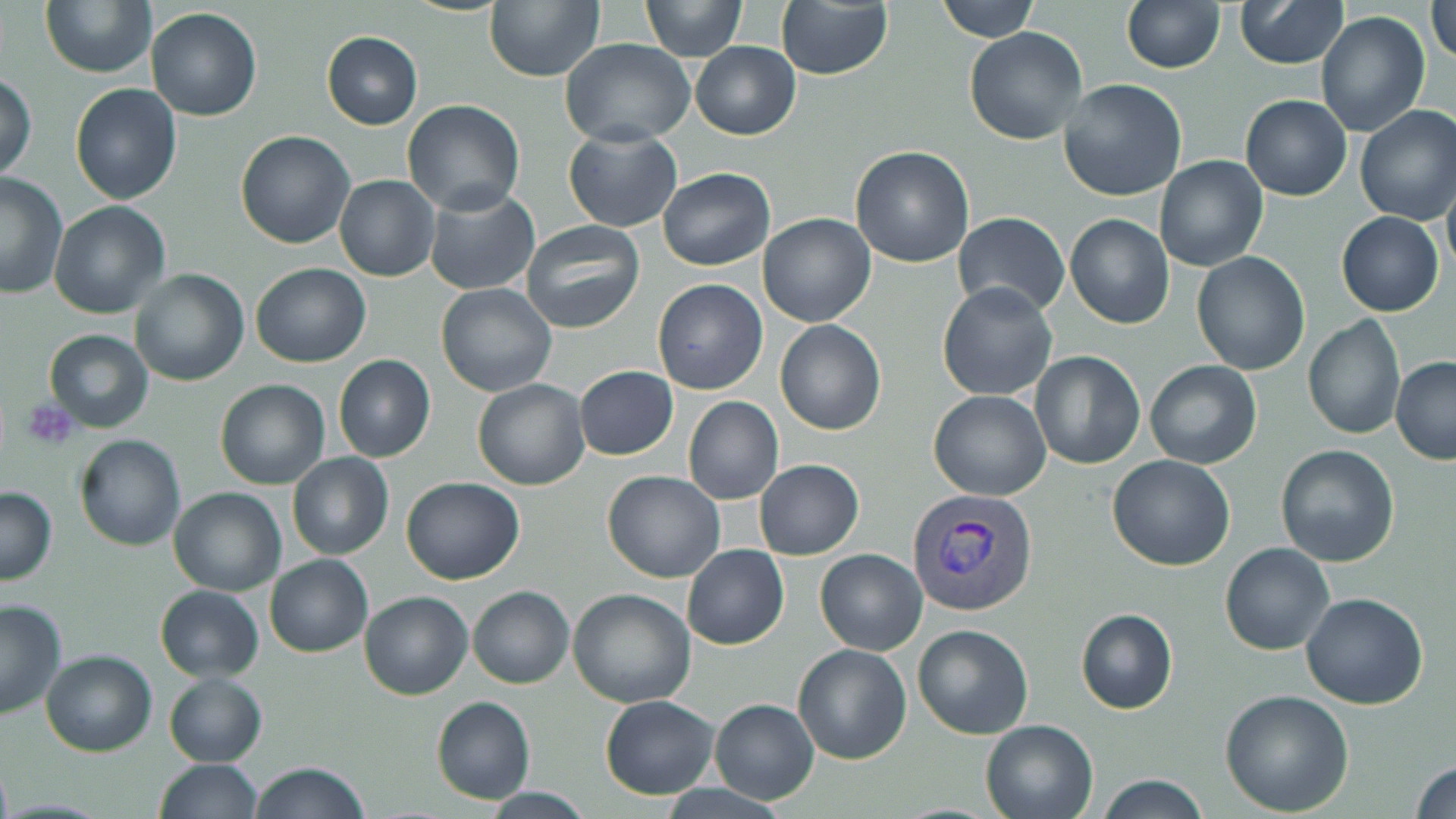

Approximate bounding boxes as named x1/y1/x2/y2 corners in pixels. Platelet locations: (x1=24, y1=401, x2=80, y2=448). Plasmodium vivax-infected red blood cell locations: (x1=905, y1=487, x2=1039, y2=617). Uninfected red blood cell locations: (x1=483, y1=0, x2=604, y2=82), (x1=641, y1=0, x2=745, y2=60), (x1=774, y1=0, x2=892, y2=80), (x1=935, y1=0, x2=1038, y2=41), (x1=1234, y1=0, x2=1347, y2=68), (x1=40, y1=1, x2=155, y2=78), (x1=1121, y1=1, x2=1225, y2=73), (x1=1430, y1=4, x2=1456, y2=62), (x1=145, y1=7, x2=263, y2=122), (x1=1316, y1=11, x2=1428, y2=136), (x1=965, y1=28, x2=1088, y2=146), (x1=321, y1=32, x2=423, y2=129), (x1=561, y1=39, x2=695, y2=148), (x1=690, y1=40, x2=801, y2=140), (x1=0, y1=73, x2=37, y2=180), (x1=1058, y1=79, x2=1188, y2=202), (x1=70, y1=83, x2=183, y2=205), (x1=1240, y1=94, x2=1352, y2=201), (x1=403, y1=100, x2=526, y2=217), (x1=1354, y1=104, x2=1456, y2=225), (x1=564, y1=128, x2=682, y2=232), (x1=234, y1=130, x2=356, y2=249), (x1=850, y1=145, x2=975, y2=267), (x1=1154, y1=156, x2=1268, y2=272), (x1=658, y1=166, x2=775, y2=271), (x1=1, y1=172, x2=68, y2=300), (x1=334, y1=175, x2=439, y2=281), (x1=1442, y1=177, x2=1456, y2=281), (x1=423, y1=185, x2=540, y2=296), (x1=48, y1=201, x2=172, y2=320), (x1=757, y1=212, x2=876, y2=326), (x1=1336, y1=212, x2=1443, y2=317), (x1=953, y1=213, x2=1070, y2=317), (x1=1065, y1=213, x2=1174, y2=328), (x1=519, y1=219, x2=646, y2=334), (x1=1191, y1=252, x2=1310, y2=374), (x1=251, y1=262, x2=371, y2=368), (x1=130, y1=268, x2=248, y2=386), (x1=652, y1=278, x2=767, y2=394), (x1=937, y1=282, x2=1058, y2=401), (x1=435, y1=283, x2=557, y2=396), (x1=1302, y1=315, x2=1405, y2=440), (x1=775, y1=320, x2=887, y2=435), (x1=44, y1=329, x2=153, y2=432), (x1=1028, y1=350, x2=1147, y2=470), (x1=333, y1=355, x2=436, y2=463), (x1=1390, y1=356, x2=1456, y2=464), (x1=1145, y1=359, x2=1262, y2=470), (x1=574, y1=365, x2=678, y2=460), (x1=472, y1=378, x2=592, y2=490), (x1=215, y1=379, x2=329, y2=489), (x1=928, y1=390, x2=1052, y2=500), (x1=682, y1=395, x2=783, y2=505), (x1=73, y1=434, x2=187, y2=551), (x1=1276, y1=445, x2=1401, y2=566), (x1=288, y1=452, x2=394, y2=561), (x1=1108, y1=454, x2=1235, y2=570), (x1=755, y1=459, x2=863, y2=559), (x1=603, y1=470, x2=725, y2=583), (x1=400, y1=475, x2=525, y2=585), (x1=0, y1=485, x2=57, y2=584), (x1=169, y1=487, x2=287, y2=596), (x1=1220, y1=542, x2=1334, y2=656), (x1=681, y1=543, x2=789, y2=650), (x1=814, y1=549, x2=927, y2=655), (x1=264, y1=554, x2=374, y2=658), (x1=155, y1=585, x2=265, y2=682), (x1=467, y1=585, x2=574, y2=688), (x1=567, y1=588, x2=696, y2=708), (x1=358, y1=590, x2=472, y2=699), (x1=1301, y1=592, x2=1429, y2=710), (x1=0, y1=597, x2=68, y2=718), (x1=1075, y1=608, x2=1178, y2=713), (x1=913, y1=623, x2=1035, y2=739), (x1=793, y1=643, x2=911, y2=765), (x1=42, y1=649, x2=158, y2=756), (x1=163, y1=672, x2=267, y2=767), (x1=1221, y1=689, x2=1354, y2=814), (x1=599, y1=694, x2=720, y2=801), (x1=432, y1=696, x2=536, y2=805), (x1=709, y1=699, x2=819, y2=804), (x1=979, y1=718, x2=1098, y2=819), (x1=152, y1=759, x2=263, y2=819), (x1=1410, y1=760, x2=1456, y2=817), (x1=247, y1=762, x2=370, y2=819), (x1=1093, y1=775, x2=1212, y2=818). Slide-level diagnosis: Plasmodium vivax. Image is 1456×819 pixels. Thin blood film. May-Grünwald-Giemsa stain. Light microscopy. One field of a larger specimen. Captured at 1000x magnification.